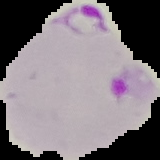
Summary:
  - Image size: 160×160 pixels
  - Image type: cell region segmented out of the field of view; surrounding area masked to black
  - Result: malaria parasites detected
  - Preparation: thin blood film